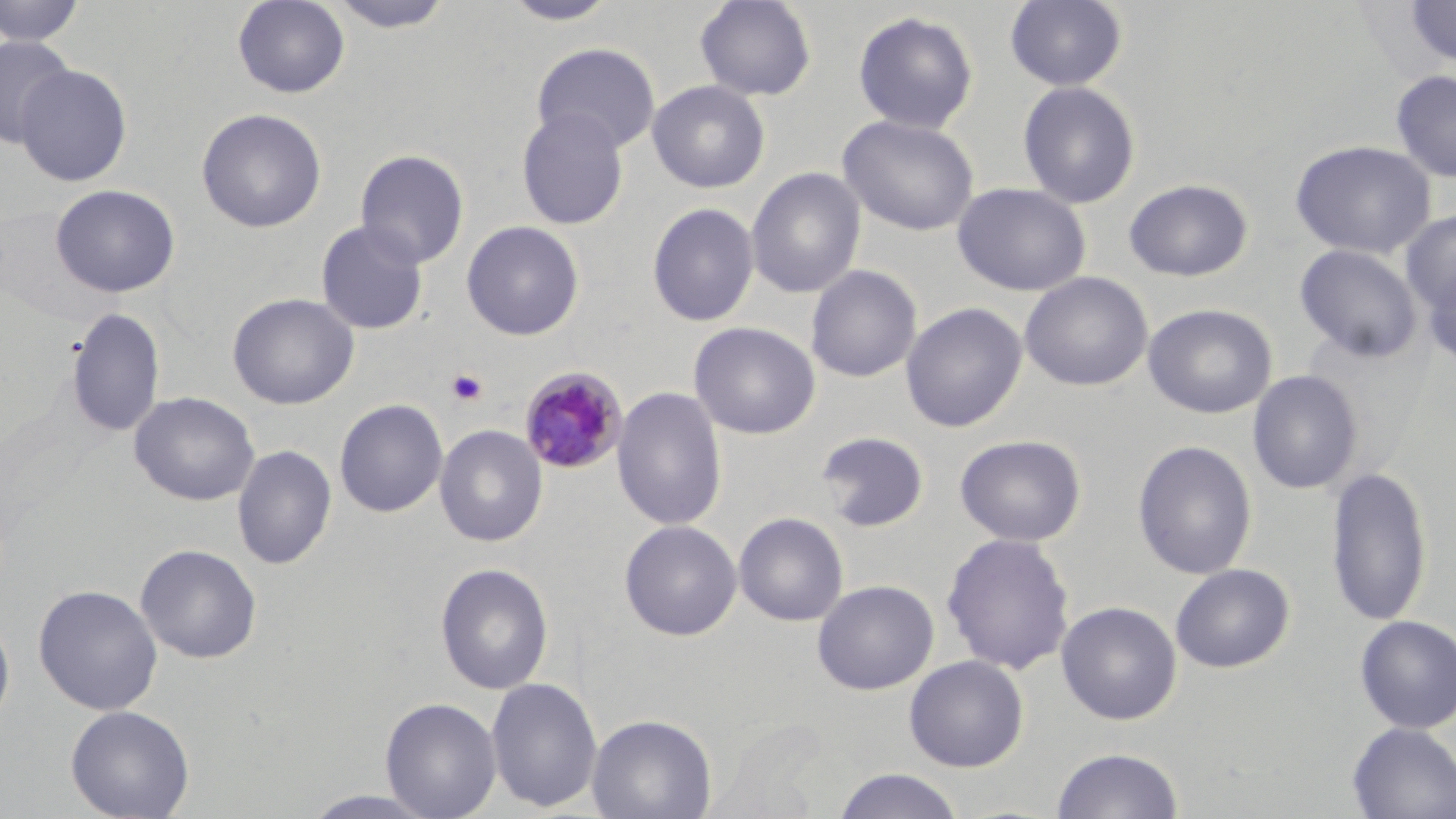

Summary:
  - Coordinate format: approximate bounding boxes as [x1, y1, x2, y2] in pixels
  - Uninfected red blood cell locations: [0, 0, 87, 46], [232, 0, 351, 99], [327, 0, 458, 33], [499, 0, 624, 26], [695, 0, 817, 102], [1005, 0, 1128, 91], [1403, 0, 1456, 69], [852, 10, 979, 134], [1, 35, 76, 148], [531, 42, 661, 154], [15, 63, 132, 187], [1390, 69, 1456, 183], [647, 80, 770, 193], [1017, 80, 1141, 209], [196, 108, 327, 233], [516, 108, 629, 230], [838, 114, 979, 235], [1290, 139, 1437, 259], [354, 149, 470, 269], [746, 167, 866, 299], [1124, 178, 1253, 282], [952, 182, 1091, 297], [50, 183, 180, 298], [646, 202, 760, 327], [1401, 210, 1456, 315], [315, 220, 429, 335], [461, 221, 584, 340], [1294, 244, 1423, 362], [805, 264, 922, 383], [1421, 265, 1456, 372], [1019, 271, 1153, 391], [227, 292, 359, 410], [901, 302, 1027, 433], [1143, 303, 1277, 419], [65, 307, 166, 438], [688, 321, 821, 440], [1247, 369, 1363, 494], [611, 386, 727, 531], [129, 391, 259, 506], [334, 399, 448, 517], [434, 424, 548, 547], [816, 430, 929, 532], [955, 434, 1086, 546], [1133, 440, 1258, 579], [232, 444, 337, 570], [1326, 466, 1432, 627], [733, 512, 849, 627], [619, 519, 742, 641], [942, 532, 1075, 675], [135, 543, 262, 664], [435, 562, 554, 695], [1170, 563, 1295, 673], [812, 579, 939, 696], [33, 584, 163, 715], [1056, 600, 1182, 725], [0, 609, 16, 729], [1354, 614, 1456, 733], [904, 655, 1029, 772], [486, 677, 602, 812], [380, 697, 502, 818], [65, 704, 195, 819], [587, 713, 717, 819], [1347, 722, 1456, 819], [1050, 747, 1185, 819], [832, 769, 966, 819], [300, 789, 441, 818]
  - Plasmodium malariae-infected red blood cell locations: [519, 366, 629, 475]
  - Platelet locations: [446, 369, 488, 406]
  - Slide-level diagnosis: Plasmodium malariae
  - Image size: 1456×819 pixels
  - Magnification: 1000x
  - Field of view: one of a larger specimen
  - Modality: light microscopy
  - Stain: May-Grünwald-Giemsa
  - Preparation: thin blood film